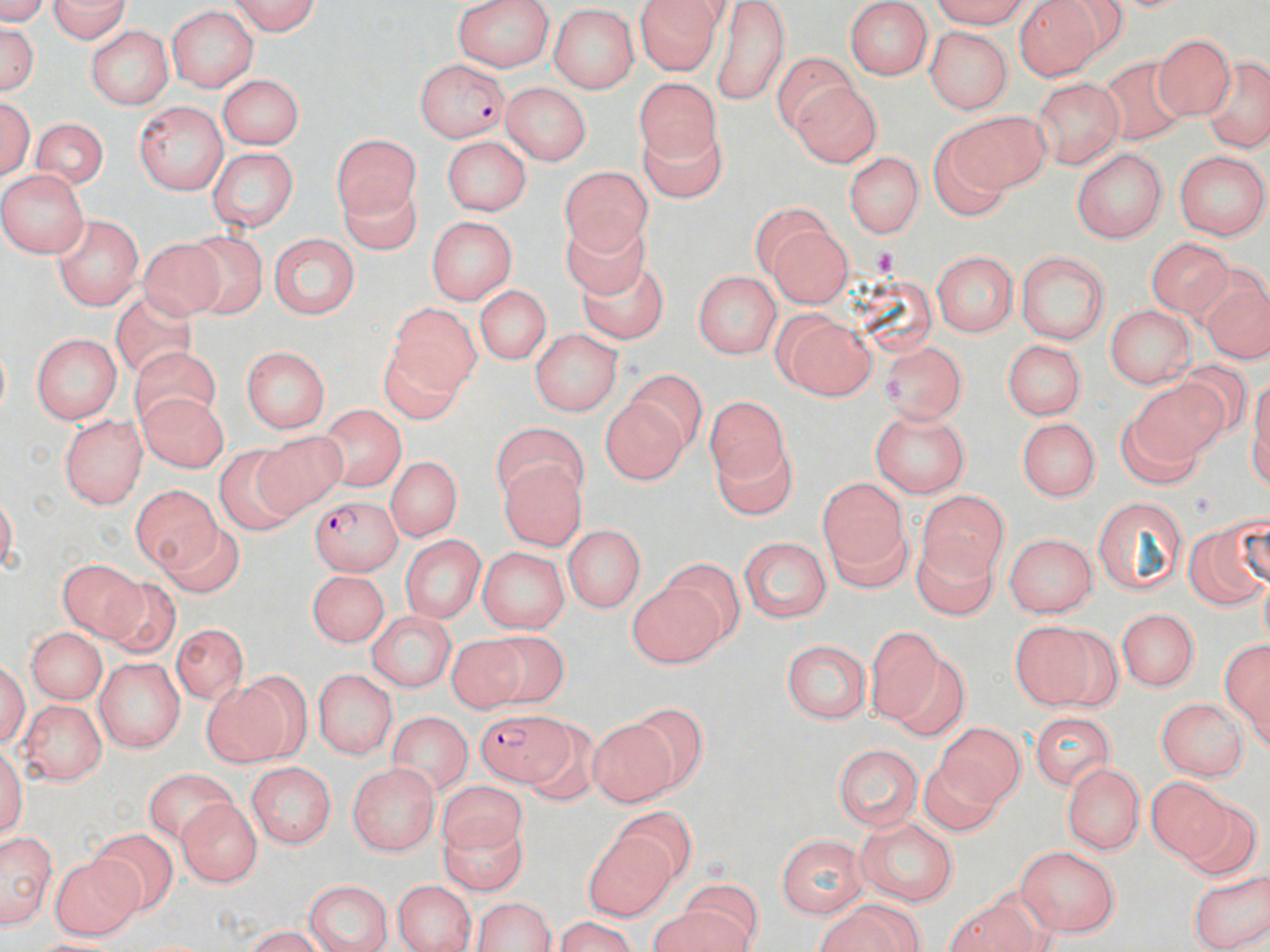
Summary:
  - Coordinate format: approximate bounding boxes as [x1, y1, x2, y2] in pixels
  - Uninfected red blood cell locations: [42, 0, 129, 43], [225, 0, 323, 35], [450, 0, 557, 73], [635, 1, 723, 75], [712, 1, 786, 109], [921, 1, 1033, 26], [1015, 2, 1105, 80], [844, 4, 933, 80], [165, 7, 261, 91], [546, 7, 641, 91], [1, 18, 40, 101], [83, 27, 175, 107], [927, 30, 1009, 111], [1156, 34, 1231, 121], [1098, 50, 1192, 146], [1202, 52, 1270, 151], [770, 55, 858, 135], [215, 72, 307, 147], [789, 76, 881, 169], [636, 80, 732, 170], [1032, 81, 1125, 170], [502, 82, 590, 168], [133, 102, 227, 192], [944, 112, 1051, 189], [29, 115, 106, 193], [630, 122, 729, 199], [325, 132, 417, 213], [440, 135, 532, 215], [206, 148, 299, 233], [1072, 148, 1164, 240], [1176, 150, 1267, 240], [842, 153, 922, 238], [559, 167, 660, 262], [0, 169, 86, 257], [340, 170, 427, 261], [750, 204, 855, 308], [556, 210, 664, 300], [53, 215, 143, 311], [426, 218, 520, 303], [181, 225, 274, 315], [268, 231, 360, 321], [1146, 233, 1228, 319], [142, 237, 225, 318], [1018, 249, 1112, 343], [931, 250, 1018, 339], [580, 263, 670, 342], [692, 271, 779, 359], [1205, 283, 1270, 364], [472, 285, 552, 367], [110, 293, 202, 370], [392, 298, 488, 399], [1106, 302, 1193, 391], [773, 310, 878, 402], [527, 330, 623, 415], [30, 332, 120, 425], [1001, 336, 1088, 421], [125, 343, 220, 417], [880, 343, 965, 425], [241, 344, 330, 431], [379, 350, 471, 425], [628, 371, 711, 450], [1122, 382, 1241, 474], [702, 392, 795, 514], [135, 395, 230, 470], [607, 399, 690, 486], [314, 405, 404, 495], [869, 408, 971, 497], [57, 414, 145, 507], [1018, 416, 1100, 505], [488, 427, 588, 508], [250, 429, 347, 513], [208, 447, 302, 535], [386, 455, 460, 542], [497, 456, 588, 546], [817, 474, 913, 589], [131, 484, 225, 575], [920, 492, 1005, 577], [1095, 498, 1192, 598], [163, 523, 241, 596], [562, 523, 646, 613], [1194, 523, 1246, 609], [1005, 533, 1098, 616], [403, 534, 485, 623], [914, 535, 993, 617], [737, 536, 831, 625], [479, 546, 570, 636], [54, 555, 151, 641], [306, 569, 387, 647], [623, 575, 726, 670], [102, 580, 180, 657], [1120, 606, 1200, 695], [367, 607, 454, 691], [1008, 620, 1123, 711], [865, 626, 937, 722], [27, 627, 105, 699], [175, 628, 247, 707], [493, 634, 573, 710], [1221, 634, 1270, 746], [450, 636, 528, 712], [782, 638, 870, 726], [93, 654, 182, 753], [898, 658, 967, 740], [310, 668, 400, 758], [199, 672, 306, 768], [1157, 696, 1246, 781], [18, 701, 105, 788], [635, 701, 706, 780], [1028, 708, 1119, 787], [390, 715, 472, 796], [589, 722, 681, 803], [937, 725, 1025, 813], [834, 745, 925, 830], [922, 758, 998, 833], [1060, 759, 1148, 854], [246, 764, 336, 847], [346, 765, 439, 856], [147, 773, 251, 840], [1149, 782, 1234, 866], [438, 784, 534, 855], [175, 800, 261, 889], [1181, 802, 1262, 881], [613, 807, 696, 881], [860, 812, 958, 906], [435, 813, 532, 894], [91, 831, 176, 911], [3, 832, 54, 928], [582, 832, 674, 921], [775, 832, 865, 920], [1015, 843, 1123, 937], [51, 854, 148, 940], [1185, 862, 1270, 951], [303, 879, 397, 951], [392, 879, 476, 952], [469, 895, 561, 951], [655, 899, 764, 952], [815, 900, 925, 952], [947, 902, 1050, 952], [547, 918, 648, 950]
  - Plasmodium falciparum-infected red blood cell locations: [417, 58, 510, 144], [312, 494, 402, 572], [477, 713, 572, 785]
  - Slide-level diagnosis: Plasmodium falciparum
  - Stain: May-Grünwald-Giemsa
  - Magnification: 1000x
  - Modality: optical microscopy
  - Image size: 1270×952 pixels
  - Field of view: single
  - Preparation: thin blood film